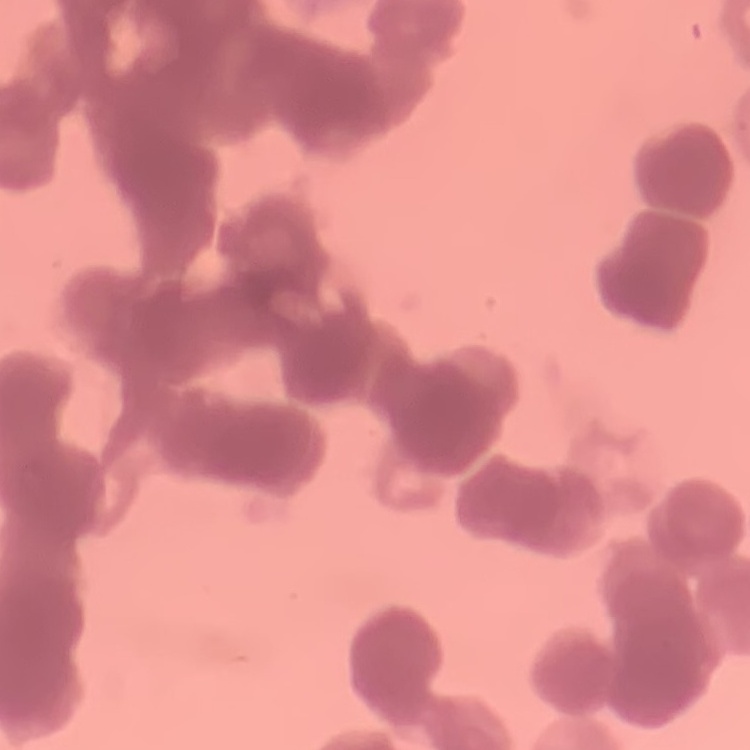

Summary:
  - Erythrocyte morphology: rouleaux formation
  - Image type: one tile cut from a larger photomicrograph
  - Preparation: thin peripheral smear
  - Stain: Field's or Giemsa